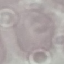 Malaria status: uninfected. Giemsa-stained preparation. Photographed with a smartphone camera at the microscope eyepiece. Cell patch, automatically extracted from a larger field of view and resized to 64 × 64 pixels. Thin smear of blood.